Describe the morphology of the red blood cells.
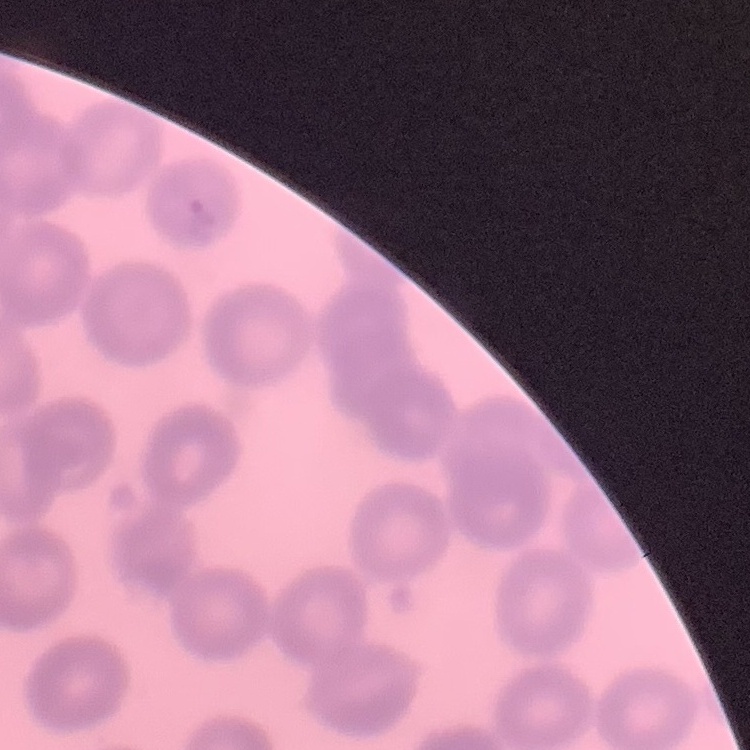

They show no rouleaux formation.

Thin blood smear. One tile cut from a larger photomicrograph. Stained with either Field's or Giemsa.